Give the extent of all Plasmodium ovale-infected red blood cells.
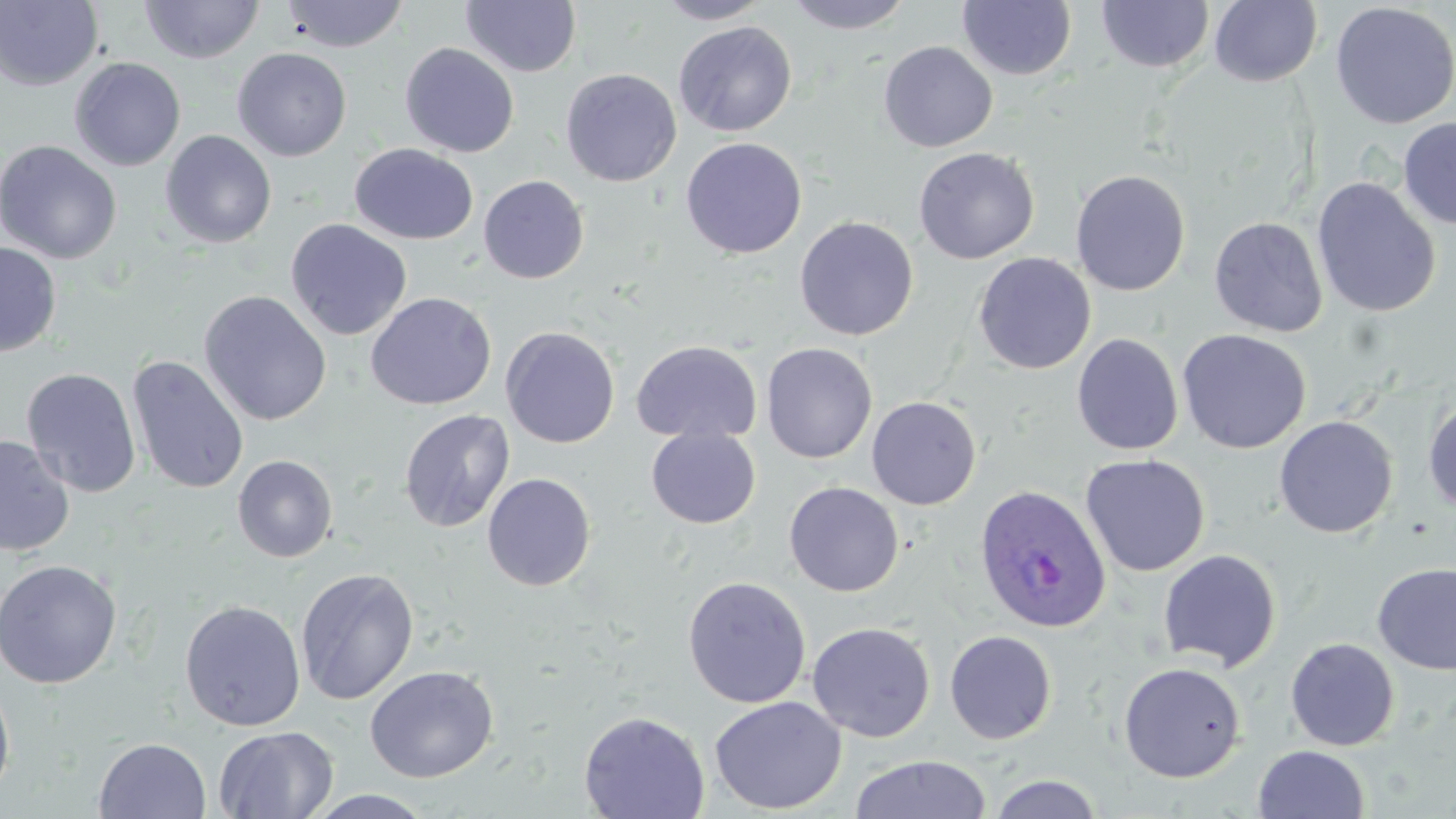
Approximate bounding boxes as (x1, y1, x2, y2) in pixels.
Plasmodium ovale-infected red blood cells: (973, 485, 1111, 634).

Summary:
  - Uninfected red blood cell locations: (140, 0, 263, 64), (279, 0, 409, 53), (655, 0, 773, 24), (786, 0, 914, 35), (1096, 0, 1213, 74), (0, 1, 104, 91), (460, 1, 582, 78), (957, 1, 1077, 81), (1209, 1, 1323, 87), (1329, 2, 1456, 129), (673, 21, 797, 136), (878, 41, 998, 153), (400, 43, 519, 157), (232, 47, 352, 162), (69, 57, 186, 172), (560, 68, 682, 187), (1398, 117, 1456, 229), (160, 130, 277, 249), (680, 137, 807, 259), (0, 140, 122, 265), (350, 144, 479, 245), (914, 147, 1040, 264), (1070, 169, 1191, 296), (478, 175, 589, 284), (1312, 177, 1441, 318), (794, 216, 919, 341), (1209, 216, 1329, 337), (285, 218, 412, 341), (0, 242, 61, 357), (972, 252, 1096, 374), (198, 290, 332, 427), (365, 292, 497, 410), (501, 326, 619, 448), (1177, 329, 1311, 454), (1071, 333, 1183, 455), (630, 340, 762, 444), (761, 342, 877, 464), (126, 355, 249, 494), (21, 367, 142, 498), (1422, 395, 1456, 516), (866, 396, 982, 509), (399, 408, 515, 533), (1274, 415, 1398, 538), (646, 428, 761, 529), (0, 434, 75, 557), (232, 454, 338, 563), (1080, 454, 1210, 577), (482, 473, 596, 591), (784, 481, 904, 596), (1157, 549, 1282, 672), (0, 559, 122, 689), (1372, 562, 1456, 676), (295, 568, 419, 705), (682, 576, 812, 709), (179, 599, 306, 731), (807, 621, 935, 742), (944, 630, 1057, 744), (1285, 638, 1400, 751), (1118, 661, 1246, 783), (364, 664, 500, 783), (0, 675, 16, 804), (710, 696, 848, 815), (579, 710, 710, 818), (213, 726, 338, 818), (93, 736, 211, 819), (1253, 745, 1371, 819), (849, 754, 993, 818), (987, 774, 1105, 818), (305, 789, 436, 818)
  - Slide-level diagnosis: Plasmodium ovale
  - Magnification: 1000x
  - Modality: optical microscopy
  - Preparation: thin blood film
  - Image size: 1456×819 pixels
  - Field of view: one of a larger specimen
  - Stain: May-Grünwald-Giemsa